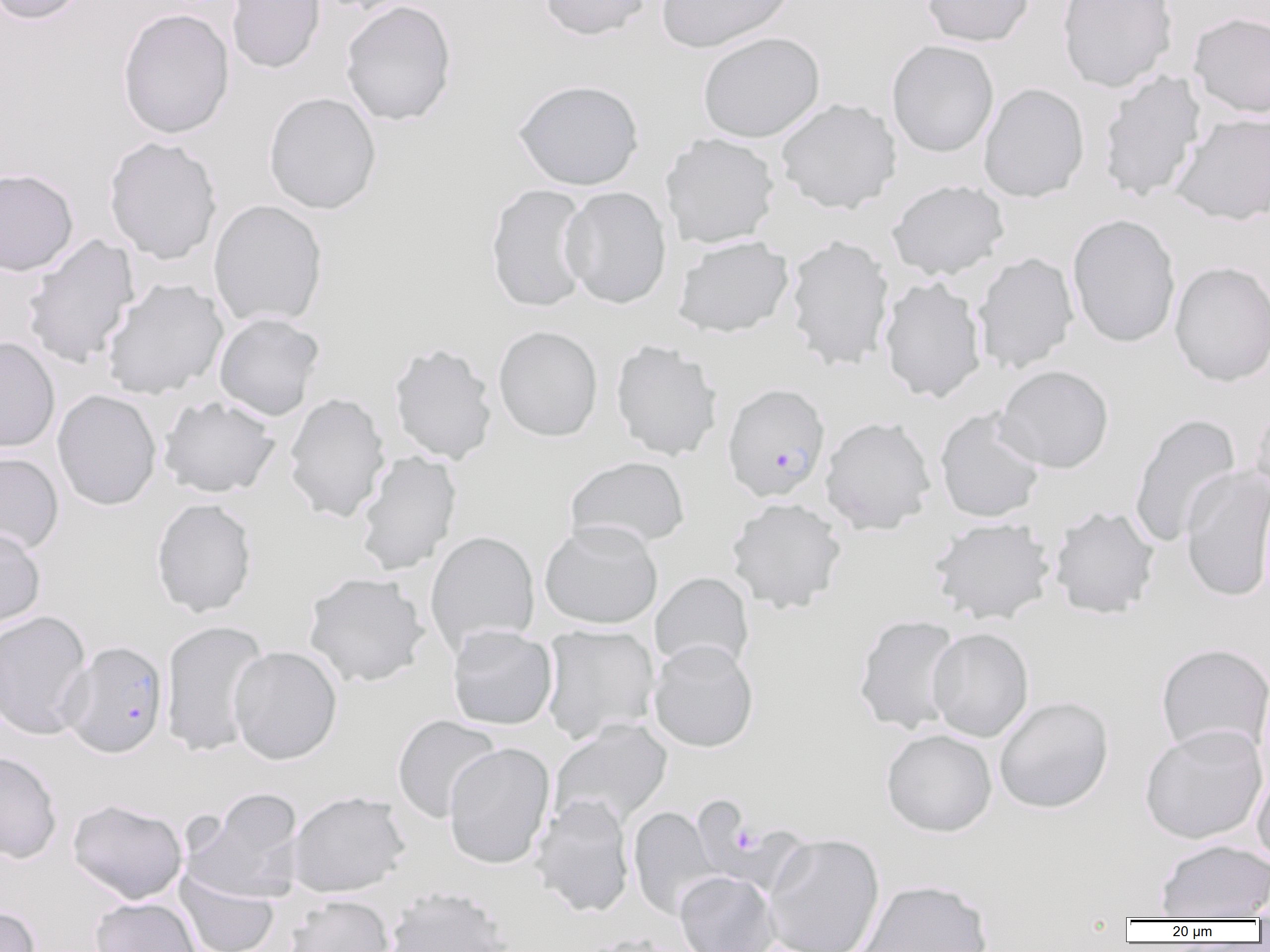

slide-level diagnosis = Plasmodium falciparum
image size = 1270×952 pixels
preparation = thin blood smear
modality = light microscopy
uninfected red blood cell locations = approximate bounding boxes as named x1/y1/x2/y2 corners in pixels: (x1=1, y1=0, x2=91, y2=25), (x1=226, y1=0, x2=326, y2=74), (x1=309, y1=0, x2=416, y2=14), (x1=539, y1=0, x2=652, y2=41), (x1=655, y1=0, x2=795, y2=53), (x1=922, y1=0, x2=1035, y2=47), (x1=1056, y1=0, x2=1178, y2=92), (x1=340, y1=1, x2=457, y2=126), (x1=117, y1=8, x2=234, y2=139), (x1=1188, y1=12, x2=1270, y2=118), (x1=697, y1=31, x2=825, y2=143), (x1=886, y1=40, x2=999, y2=157), (x1=1098, y1=69, x2=1206, y2=203), (x1=512, y1=79, x2=644, y2=190), (x1=978, y1=82, x2=1090, y2=202), (x1=263, y1=92, x2=381, y2=214), (x1=775, y1=98, x2=901, y2=214), (x1=1170, y1=111, x2=1270, y2=225), (x1=660, y1=133, x2=780, y2=248), (x1=103, y1=137, x2=223, y2=264), (x1=0, y1=168, x2=79, y2=276), (x1=887, y1=179, x2=1009, y2=280), (x1=485, y1=183, x2=592, y2=313), (x1=560, y1=186, x2=672, y2=309), (x1=208, y1=200, x2=328, y2=328), (x1=1067, y1=213, x2=1181, y2=348), (x1=23, y1=234, x2=140, y2=369), (x1=673, y1=235, x2=794, y2=338), (x1=784, y1=235, x2=894, y2=372), (x1=971, y1=252, x2=1079, y2=374), (x1=1169, y1=261, x2=1270, y2=387), (x1=879, y1=275, x2=986, y2=403), (x1=101, y1=278, x2=228, y2=400), (x1=214, y1=312, x2=324, y2=421), (x1=493, y1=325, x2=603, y2=441), (x1=0, y1=336, x2=60, y2=453), (x1=611, y1=340, x2=723, y2=461), (x1=388, y1=341, x2=497, y2=465), (x1=995, y1=365, x2=1114, y2=473), (x1=52, y1=389, x2=162, y2=511), (x1=283, y1=392, x2=390, y2=523), (x1=158, y1=395, x2=281, y2=498), (x1=1250, y1=396, x2=1270, y2=508), (x1=935, y1=408, x2=1046, y2=523), (x1=1128, y1=413, x2=1241, y2=549), (x1=820, y1=416, x2=936, y2=534), (x1=355, y1=450, x2=462, y2=575), (x1=0, y1=451, x2=64, y2=555), (x1=565, y1=455, x2=690, y2=550), (x1=1180, y1=466, x2=1270, y2=602), (x1=726, y1=497, x2=847, y2=614), (x1=151, y1=498, x2=257, y2=618), (x1=1049, y1=505, x2=1160, y2=619), (x1=929, y1=517, x2=1055, y2=624), (x1=539, y1=519, x2=663, y2=629), (x1=0, y1=527, x2=46, y2=629), (x1=425, y1=530, x2=540, y2=654), (x1=303, y1=572, x2=430, y2=688), (x1=650, y1=572, x2=754, y2=675), (x1=0, y1=610, x2=93, y2=740), (x1=853, y1=614, x2=963, y2=735), (x1=159, y1=620, x2=270, y2=756), (x1=540, y1=624, x2=660, y2=745), (x1=446, y1=626, x2=558, y2=730), (x1=927, y1=627, x2=1034, y2=742), (x1=648, y1=639, x2=759, y2=752), (x1=1155, y1=642, x2=1270, y2=759), (x1=228, y1=645, x2=343, y2=765), (x1=993, y1=696, x2=1114, y2=813), (x1=392, y1=715, x2=502, y2=823), (x1=549, y1=719, x2=673, y2=832), (x1=1140, y1=724, x2=1268, y2=844), (x1=881, y1=728, x2=997, y2=837), (x1=443, y1=742, x2=555, y2=870), (x1=0, y1=750, x2=62, y2=863), (x1=1251, y1=768, x2=1270, y2=869), (x1=184, y1=787, x2=305, y2=903), (x1=287, y1=790, x2=409, y2=898), (x1=530, y1=795, x2=635, y2=917), (x1=67, y1=798, x2=187, y2=904), (x1=628, y1=806, x2=723, y2=921), (x1=763, y1=832, x2=885, y2=952), (x1=1155, y1=839, x2=1270, y2=920), (x1=174, y1=867, x2=280, y2=952), (x1=674, y1=871, x2=779, y2=952), (x1=855, y1=879, x2=993, y2=952), (x1=384, y1=885, x2=515, y2=952), (x1=1251, y1=886, x2=1270, y2=924), (x1=283, y1=895, x2=395, y2=952), (x1=89, y1=897, x2=201, y2=952), (x1=0, y1=904, x2=41, y2=952)
platelet locations = approximate bounding boxes as named x1/y1/x2/y2 corners in pixels: (x1=733, y1=824, x2=761, y2=855)
magnification = 1000x
Plasmodium falciparum-infected red blood cell locations = approximate bounding boxes as named x1/y1/x2/y2 corners in pixels: (x1=722, y1=383, x2=831, y2=501), (x1=62, y1=641, x2=169, y2=758)
field of view = one of a larger specimen